Assess this cell for malaria.
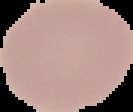
It is uninfected.

image size = 133×112 pixels
preparation = thin blood smear
image type = segmented cell region on a black background